Locate every uninfected red blood cell.
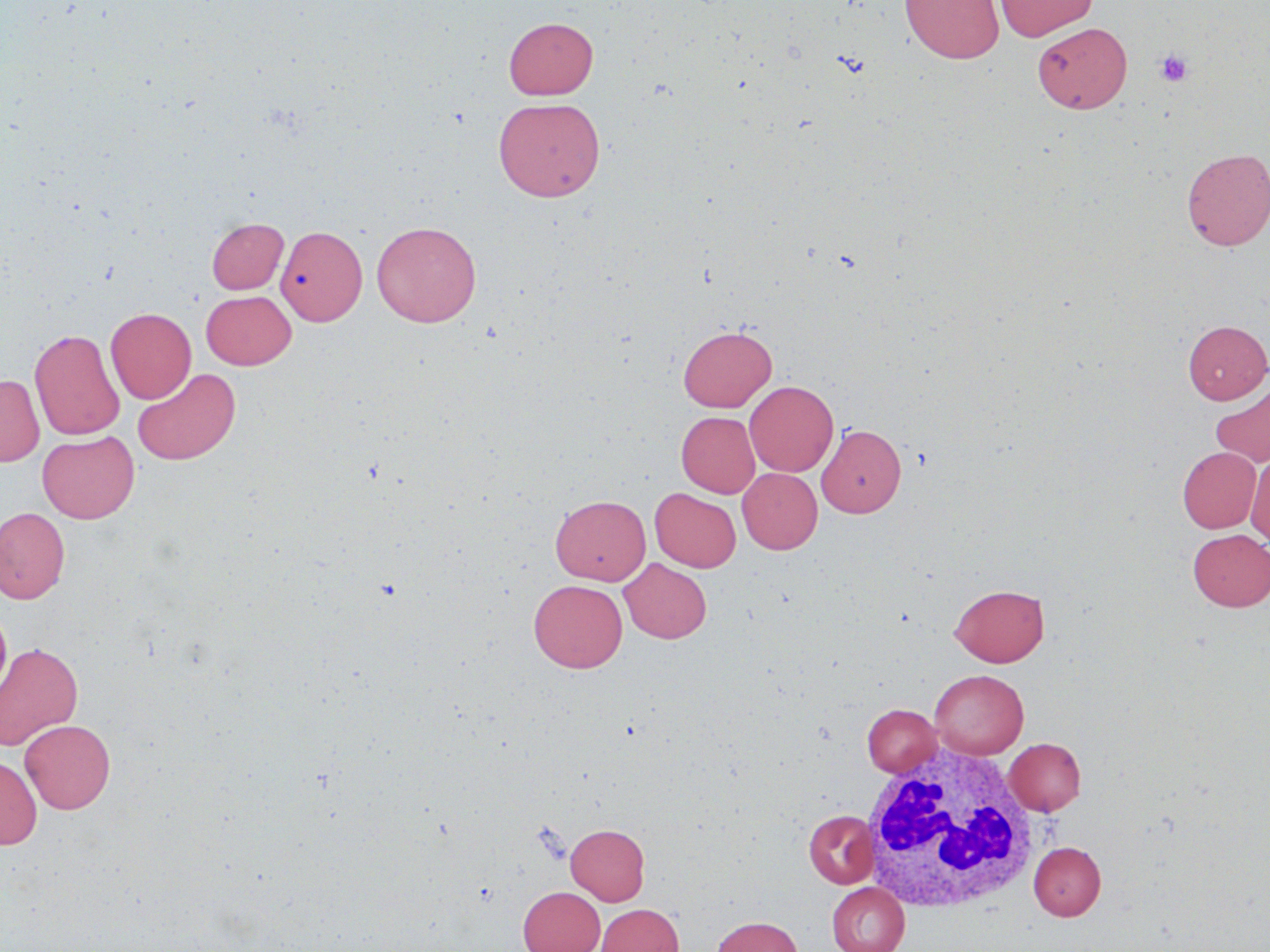
Approximate bounding boxes as (x1, y1, x2, y2) in pixels.
Uninfected red blood cells: (900, 0, 1004, 64), (993, 0, 1098, 41), (504, 17, 598, 99), (1033, 22, 1132, 113), (493, 97, 605, 201), (1181, 148, 1270, 250), (207, 218, 288, 294), (371, 220, 481, 327), (276, 225, 367, 326), (201, 290, 297, 370), (105, 307, 196, 403), (1183, 320, 1270, 403), (678, 325, 777, 411), (30, 327, 124, 440), (132, 367, 240, 465), (0, 374, 44, 466), (745, 380, 838, 476), (1210, 382, 1270, 468), (677, 411, 760, 497), (817, 424, 906, 517), (37, 431, 139, 523), (1178, 447, 1261, 533), (1246, 454, 1270, 545), (738, 468, 822, 554), (650, 488, 741, 572), (550, 494, 651, 585), (0, 507, 70, 604), (1187, 529, 1270, 611), (619, 558, 711, 643), (528, 580, 627, 672), (950, 583, 1050, 667), (0, 606, 12, 702), (0, 642, 83, 750), (930, 670, 1028, 758), (863, 704, 942, 777), (19, 719, 116, 813), (1004, 738, 1086, 815), (0, 756, 42, 849), (804, 810, 879, 888), (566, 824, 649, 905), (1029, 841, 1106, 920), (827, 882, 909, 952), (518, 886, 604, 952), (596, 903, 683, 952), (712, 916, 803, 952).

Platelet locations: (1154, 48, 1194, 87). White blood cell locations: (859, 745, 1043, 915). Slide-level diagnosis: negative for blood parasites. Single field of view. Thin blood film. May-Grünwald-Giemsa-stained preparation. Image is 1270×952 pixels. Captured at 1000x magnification. Optical microscopy.